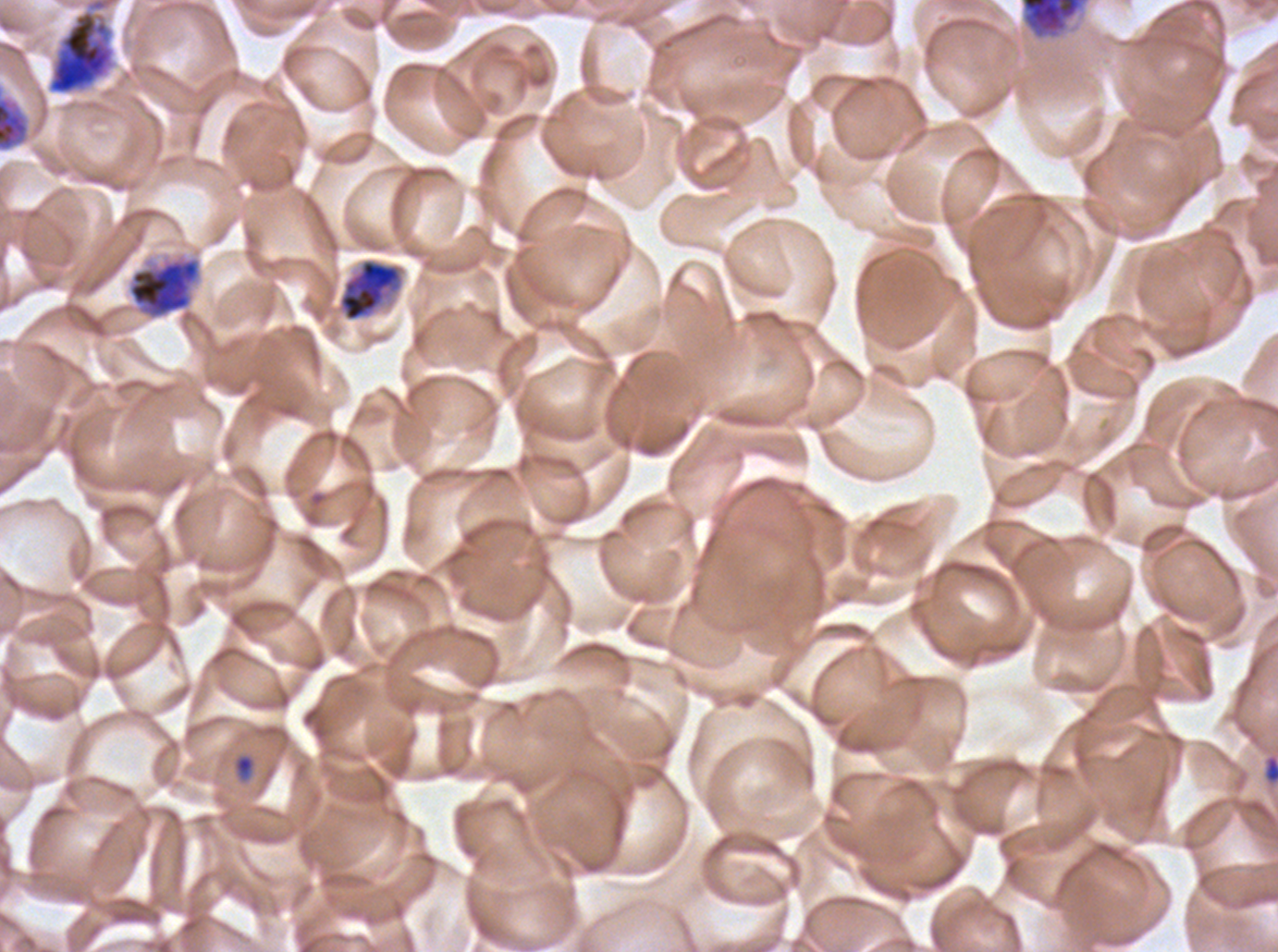
stain: Giemsa
life_cycle_stages_observed: ring, early schizont, late schizont
preparation: thin blood film
field_of_view: sub-image separated from a larger composite
early_schizont_locations: 'approximate bounding boxes as {x1, y1, x2, y2} in pixels: {46, 0, 117, 95}, {1020, 0, 1085, 39}, {337, 257, 405, 323}, {128, 258, 200, 318}'
specimen: ex-vivo P. falciparum culture from a patient in The Gambia, grown for 24 to 48 hours
image_size: 1278×952 pixels
ring_locations: 'approximate bounding boxes as {x1, y1, x2, y2} in pixels: {231, 752, 257, 785}, {1262, 753, 1277, 786}'
late_schizont_locations: 'approximate bounding boxes as {x1, y1, x2, y2} in pixels: {0, 96, 30, 152}'